Identify the blood parasite species.
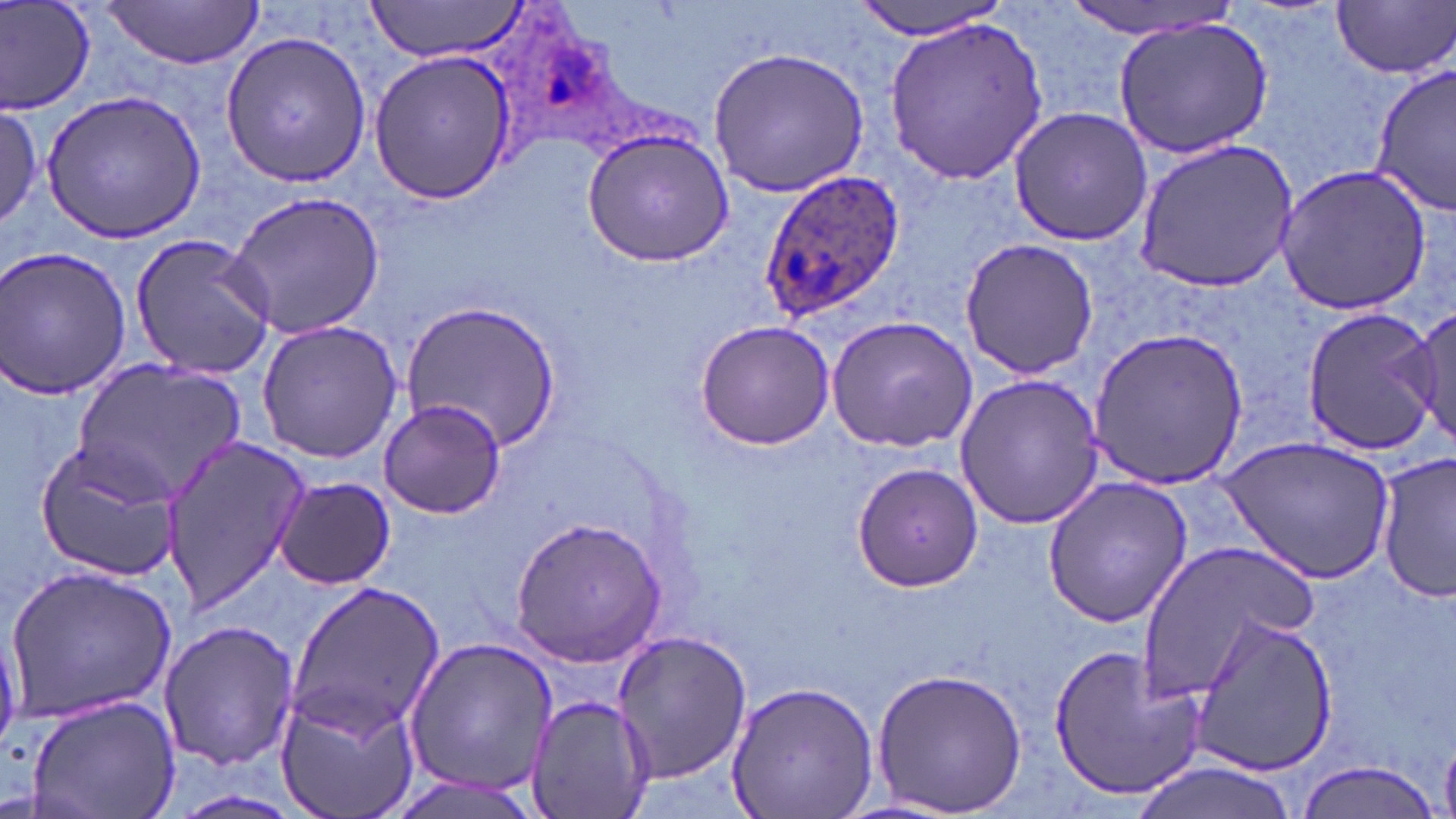
Plasmodium ovale.

{
  "stain": "May-Grünwald-Giemsa",
  "plasmodium_ovale_infected_red_blood_cell_locations": "approximate bounding boxes as named x1/y1/x2/y2 corners in pixels: (x1=760, y1=169, x2=906, y2=320)",
  "preparation": "thin blood smear",
  "magnification": "1000x",
  "modality": "optical microscopy",
  "uninfected_red_blood_cell_locations": "approximate bounding boxes as named x1/y1/x2/y2 corners in pixels: (x1=1, y1=0, x2=97, y2=116), (x1=368, y1=0, x2=531, y2=62), (x1=854, y1=0, x2=1011, y2=39), (x1=1331, y1=1, x2=1455, y2=78), (x1=1060, y1=2, x2=1241, y2=38), (x1=98, y1=3, x2=265, y2=69), (x1=1112, y1=14, x2=1276, y2=160), (x1=885, y1=15, x2=1049, y2=184), (x1=220, y1=29, x2=375, y2=187), (x1=707, y1=46, x2=871, y2=197), (x1=368, y1=50, x2=516, y2=202), (x1=1370, y1=65, x2=1456, y2=216), (x1=40, y1=90, x2=206, y2=242), (x1=0, y1=103, x2=43, y2=232), (x1=1009, y1=105, x2=1153, y2=247), (x1=582, y1=127, x2=735, y2=266), (x1=1133, y1=139, x2=1299, y2=292), (x1=1275, y1=165, x2=1432, y2=314), (x1=223, y1=190, x2=387, y2=339), (x1=130, y1=235, x2=276, y2=378), (x1=959, y1=238, x2=1099, y2=378), (x1=0, y1=247, x2=134, y2=400), (x1=402, y1=298, x2=561, y2=451), (x1=1300, y1=306, x2=1439, y2=456), (x1=1410, y1=306, x2=1454, y2=452), (x1=826, y1=315, x2=979, y2=451), (x1=256, y1=320, x2=405, y2=462), (x1=695, y1=320, x2=835, y2=451), (x1=1088, y1=325, x2=1249, y2=488), (x1=73, y1=360, x2=245, y2=501), (x1=953, y1=374, x2=1104, y2=530), (x1=377, y1=398, x2=506, y2=518), (x1=157, y1=433, x2=311, y2=613), (x1=1221, y1=438, x2=1396, y2=585), (x1=34, y1=440, x2=184, y2=581), (x1=1376, y1=452, x2=1455, y2=604), (x1=852, y1=461, x2=984, y2=593), (x1=1041, y1=476, x2=1194, y2=627), (x1=273, y1=477, x2=397, y2=590), (x1=511, y1=517, x2=669, y2=666), (x1=1135, y1=537, x2=1322, y2=706), (x1=7, y1=564, x2=178, y2=720), (x1=287, y1=581, x2=447, y2=742), (x1=1186, y1=611, x2=1339, y2=775), (x1=156, y1=617, x2=299, y2=773), (x1=610, y1=627, x2=750, y2=784), (x1=402, y1=635, x2=558, y2=797), (x1=1047, y1=643, x2=1207, y2=801), (x1=871, y1=665, x2=1028, y2=815), (x1=725, y1=680, x2=880, y2=819), (x1=276, y1=684, x2=421, y2=819), (x1=23, y1=693, x2=181, y2=819), (x1=524, y1=694, x2=655, y2=819), (x1=1120, y1=758, x2=1304, y2=819), (x1=1293, y1=759, x2=1444, y2=819), (x1=381, y1=772, x2=545, y2=819)",
  "image_size": "1456×819 pixels",
  "field_of_view": "single"
}